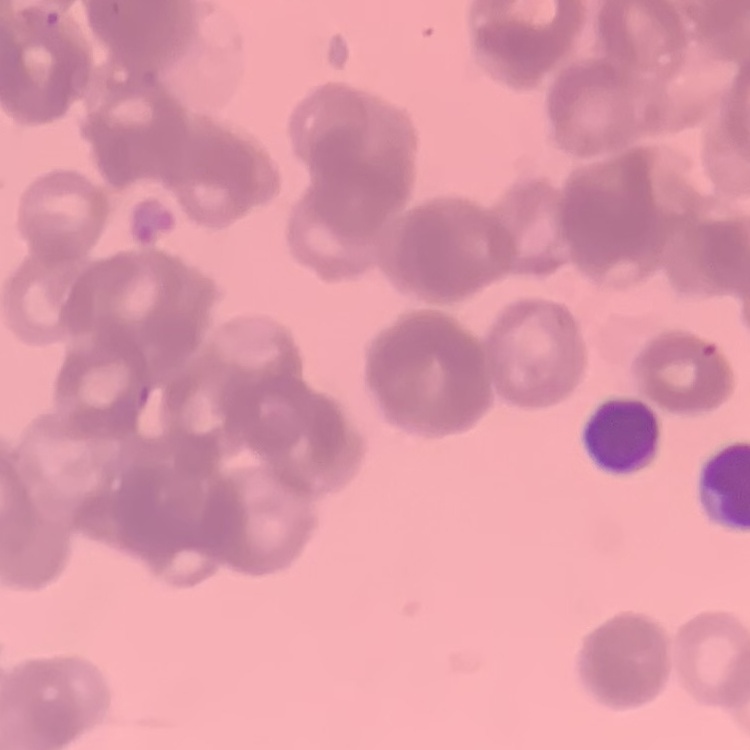

Summary:
  - Erythrocyte morphology: rouleaux formation
  - Image type: one tile cut from a larger photomicrograph
  - Stain: Field's or Giemsa
  - Preparation: thin peripheral smear